Assess the morphology of the red blood cells.
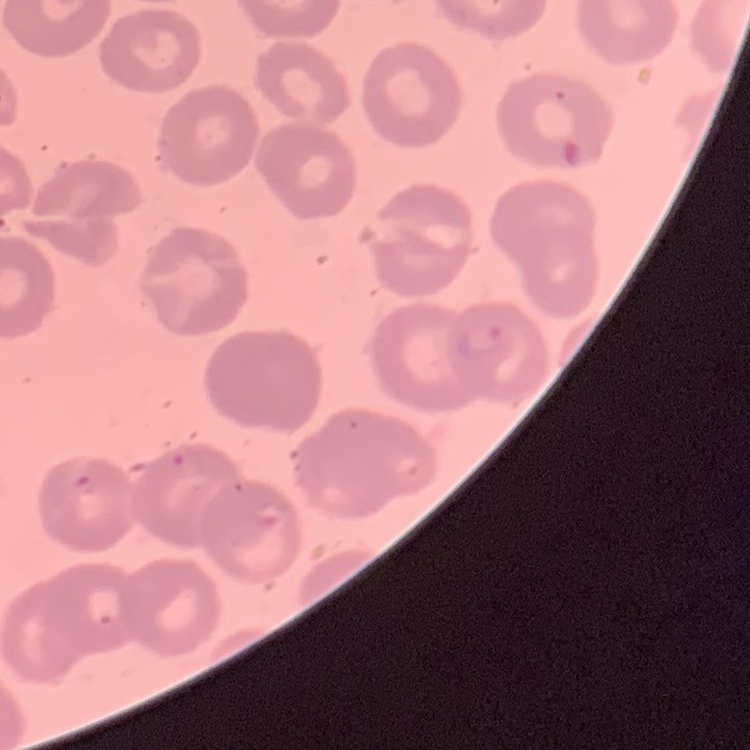
They show no rouleaux formation.

Summary:
  - Stain: Field's or Giemsa
  - Image type: one tile cut from a larger photomicrograph
  - Preparation: thin blood smear